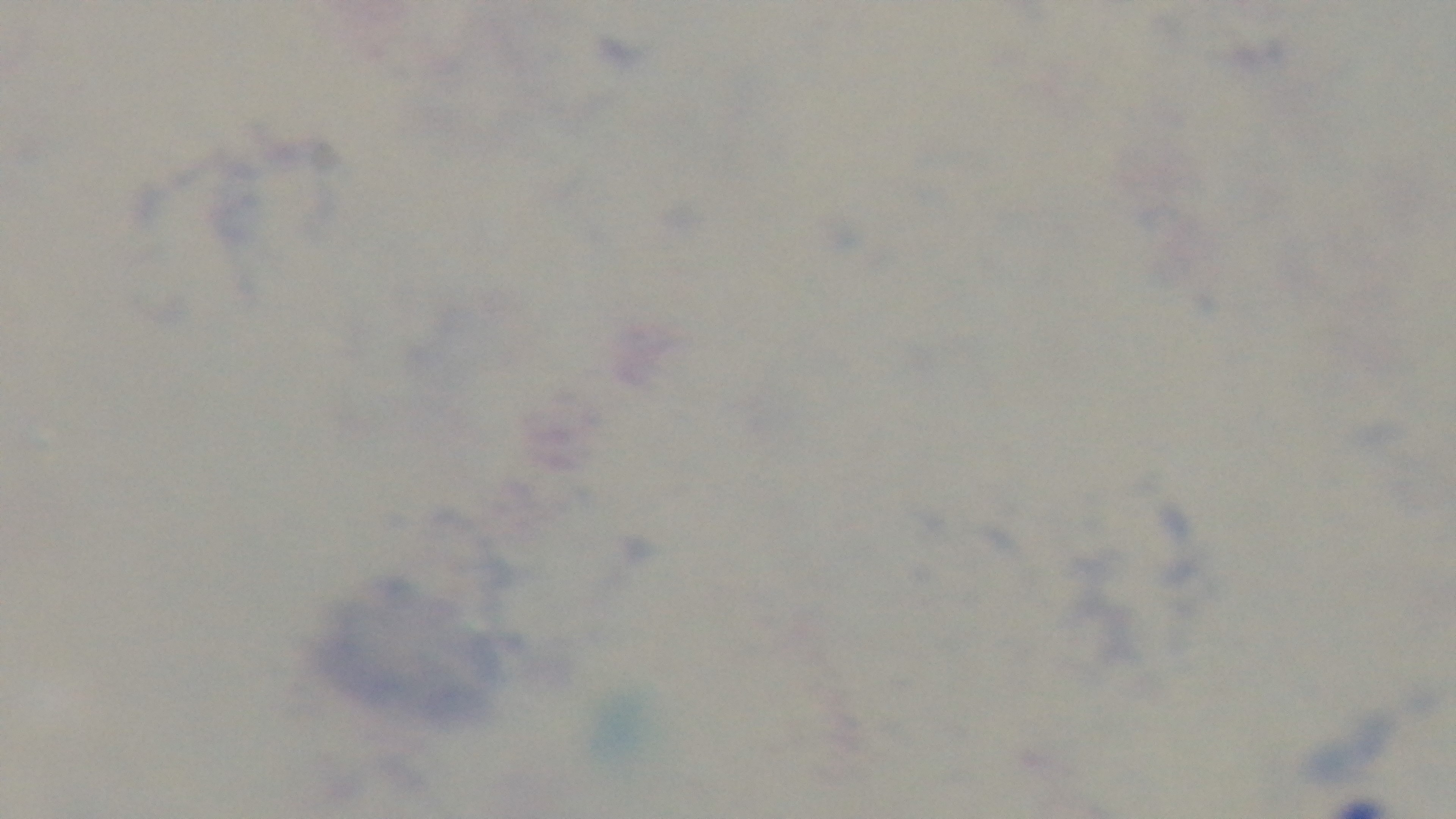

Summary:
  - Modality: light microscopy
  - Capture: mounted 4K digital camera
  - Field of view: single
  - Objective: 100x oil immersion
  - Malaria status: uninfected
  - Stain: Giemsa
  - Preparation: thick